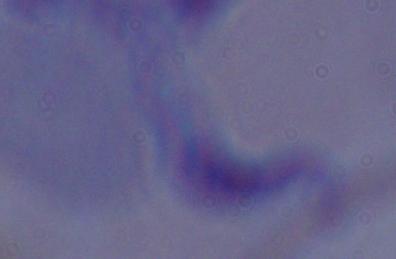
Captured at 1000x magnification. A trypanosome is shown. Photomicrograph.